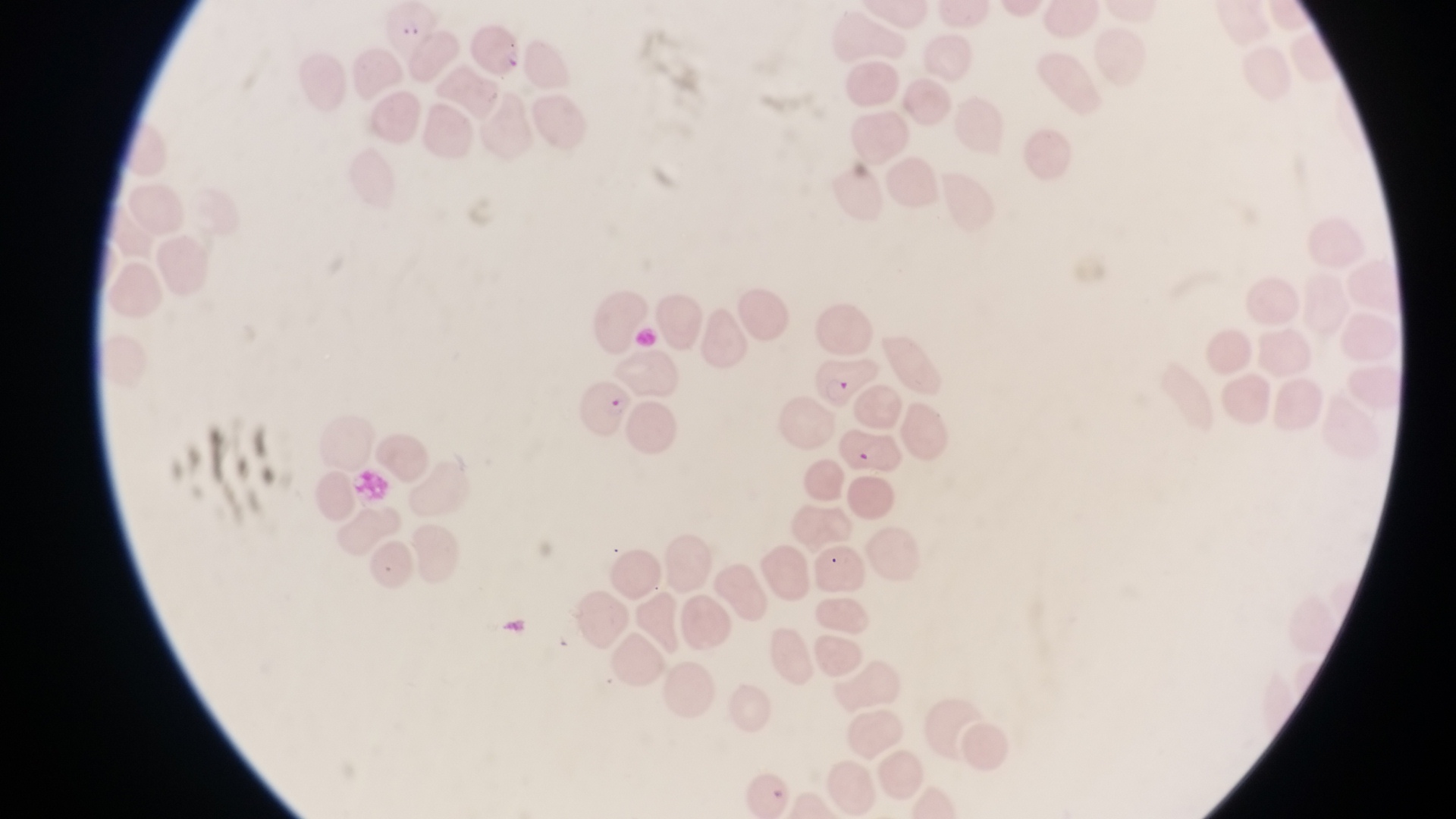 Approximate bounding boxes as [left, top, right, bottom] in pixels. Parasitised red blood cell locations: [378, 6, 445, 62], [817, 356, 876, 409], [579, 381, 631, 436], [836, 428, 913, 480]. Artifact (platelet-like body, stain precipitate, or debris) locations: [497, 42, 523, 75], [821, 548, 850, 578]. Thin blood film. Collected in Uganda. One field of view. Magnification of 1000x. Image is 1456×819 pixels. Photographed through the eyepiece of an Olympus CX-23 microscope with a smartphone camera.